Describe the morphology of the red blood cells.
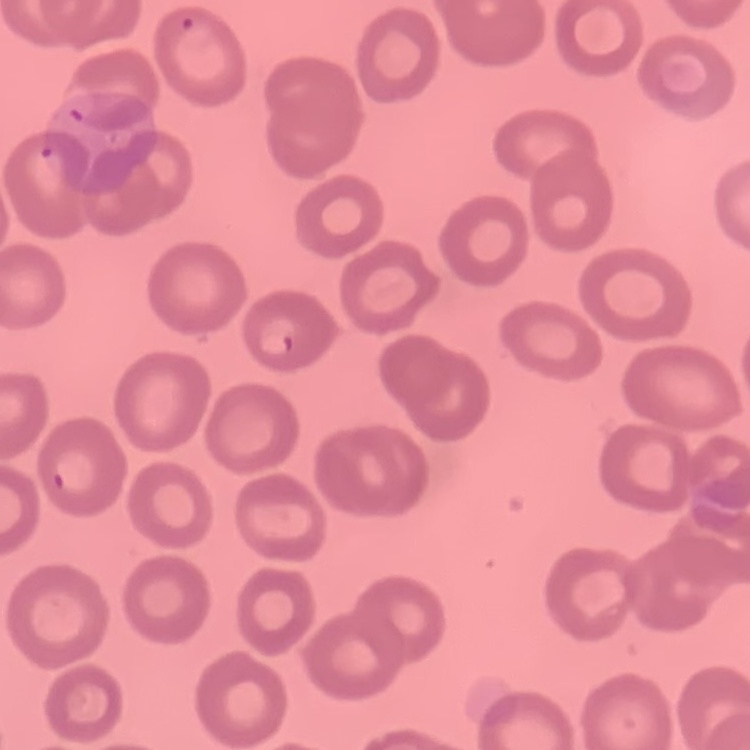
They show no rouleaux formation.

Summary:
  - Stain: Field's or Giemsa
  - Image type: square crop of a larger photomicrograph
  - Preparation: thin blood film